Identify the blood parasite species.
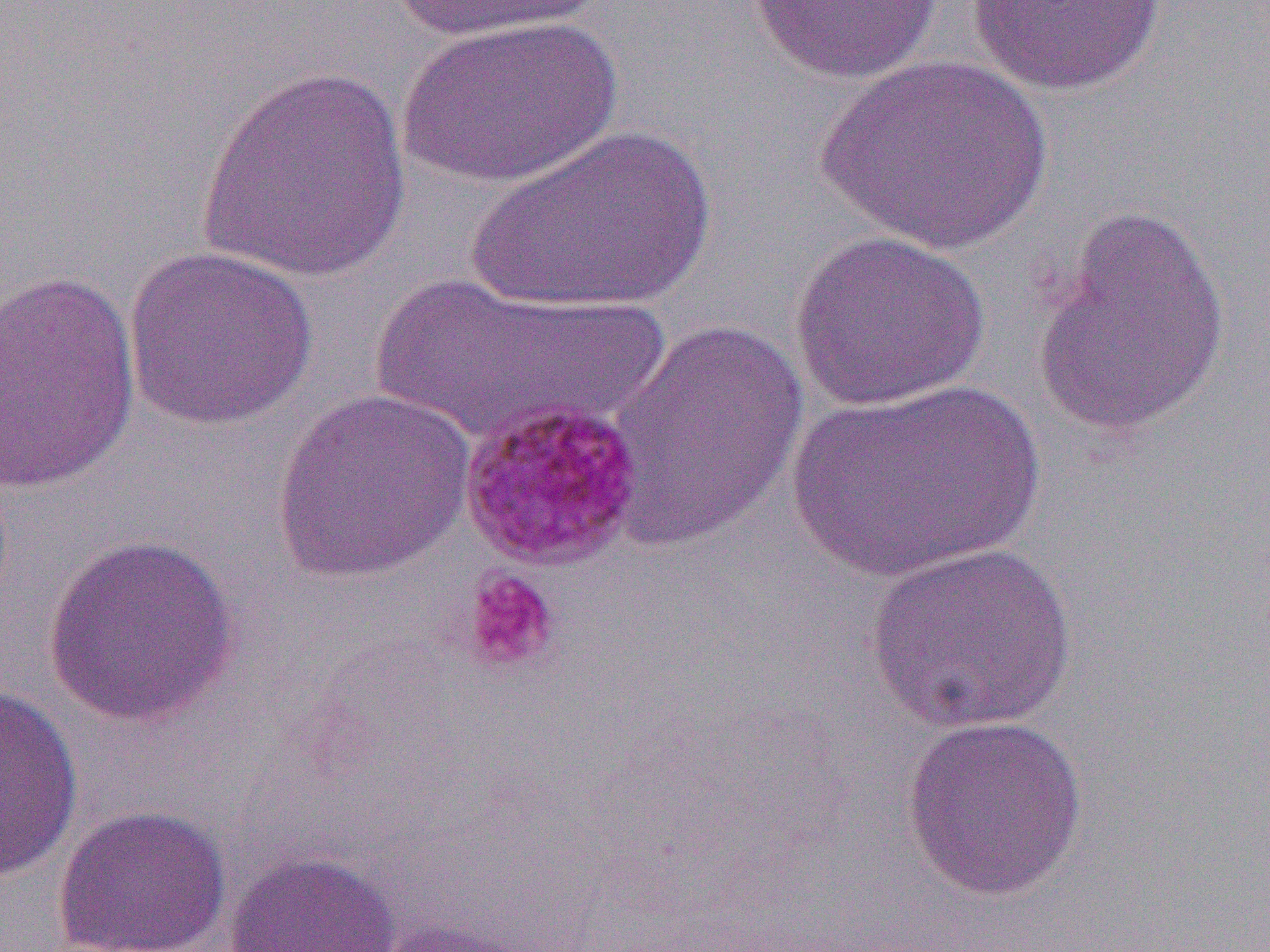
Plasmodium malariae.

Summary:
  - Coordinate format: approximate bounding boxes as (x1,y1)-(x2,y2) corner pairs in pixels
  - Platelet locations: (461,569)-(561,673)
  - Plasmodium malariae-infected red blood cell locations: (457,396)-(648,572)
  - Uninfected red blood cell locations: (967,0)-(1167,98), (384,1)-(607,46), (746,1)-(942,84), (397,15)-(622,191), (817,54)-(1054,255), (196,65)-(411,284), (463,123)-(719,315), (1031,206)-(1232,439), (788,229)-(991,412), (122,245)-(319,432), (1,269)-(141,497), (373,273)-(654,448), (607,317)-(809,548), (785,378)-(1046,584), (271,388)-(477,585), (42,532)-(242,728), (862,542)-(1080,735), (0,685)-(84,881), (899,714)-(1089,900), (52,804)-(232,952), (223,850)-(401,952), (373,915)-(546,952)
  - Magnification: 1000x
  - Modality: light microscopy
  - Field of view: one of a larger specimen
  - Image size: 1270×952 pixels
  - Preparation: thin blood film